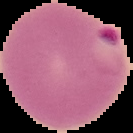

{
  "preparation": "thin blood film",
  "malaria_status": "parasitized",
  "image_size": "133×133 pixels",
  "image_type": "segmented cell region on a black background"
}